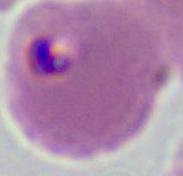 Captured at either 400x or 1000x magnification. Micrograph. A Plasmodium parasite is seen.